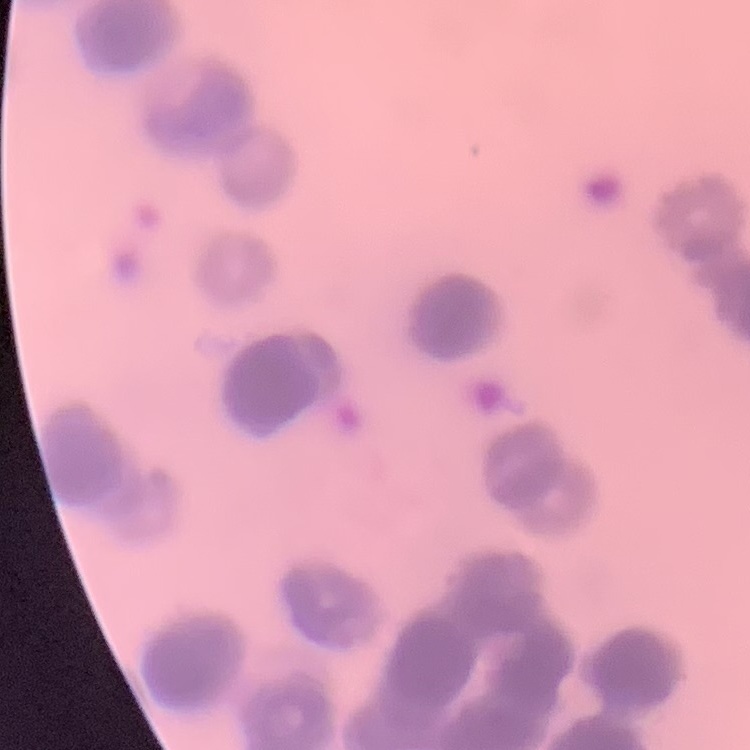 The red blood cells exhibit rouleaux formation. Field's or Giemsa stain. Thin blood film. Square crop of a larger photomicrograph.